Outline each Plasmodium ovale-infected red blood cell.
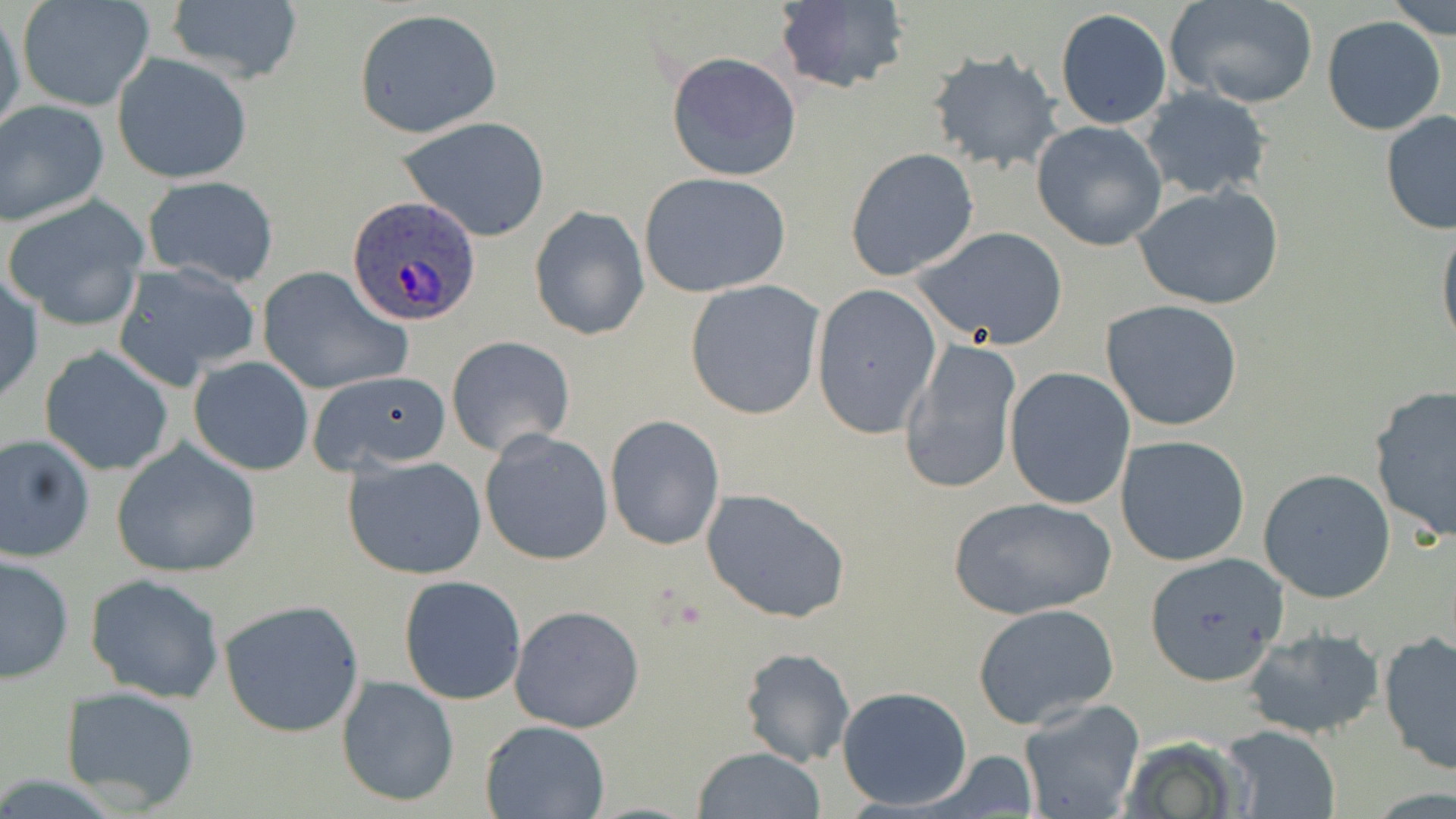

Approximate bounding boxes as (x1,y1)-(x2,y2) corner pairs in pixels.
Plasmodium ovale-infected red blood cells: (346,196)-(483,326).

slide_level_diagnosis: Plasmodium ovale
stain: May-Grünwald-Giemsa
field_of_view: single
modality: light microscopy
preparation: thin blood film
image_size: 1456×819 pixels
uninfected_red_blood_cell_locations: 'approximate bounding boxes as (x1,y1)-(x2,y2) corner pairs in pixels: (772,0)-(911,95), (1163,0)-(1319,109), (1384,0)-(1454,41), (162,1)-(305,84), (14,4)-(154,113), (0,8)-(25,146), (352,8)-(502,138), (1054,8)-(1171,129), (1321,16)-(1448,137), (927,50)-(1064,173), (666,51)-(803,181), (113,54)-(252,185), (1137,86)-(1274,200), (0,102)-(108,225), (1379,109)-(1456,234), (397,115)-(552,242), (1031,120)-(1168,250), (845,148)-(980,283), (638,172)-(792,298), (142,176)-(280,287), (1132,185)-(1284,310), (2,194)-(152,331), (529,206)-(650,342), (1436,220)-(1456,355), (913,226)-(1069,349), (112,261)-(261,390), (256,265)-(412,396), (1,274)-(43,409), (685,280)-(824,420), (811,283)-(941,437), (1100,299)-(1244,432), (446,335)-(576,460), (900,338)-(1023,496), (39,345)-(175,474), (188,356)-(315,476), (1005,366)-(1136,509), (304,369)-(456,475), (1368,385)-(1455,542), (605,414)-(726,549), (481,430)-(613,566), (0,434)-(95,563), (1116,435)-(1251,567), (110,438)-(264,578), (342,453)-(488,580), (1259,468)-(1396,602), (701,487)-(850,623), (948,496)-(1118,619), (1,552)-(74,683), (1144,552)-(1288,684), (85,573)-(226,704), (398,575)-(526,705), (218,598)-(366,737), (972,603)-(1120,730), (509,604)-(645,734), (1242,626)-(1386,741), (1378,634)-(1456,776), (739,646)-(854,768), (334,674)-(459,808), (59,685)-(200,812), (837,686)-(973,811), (1017,698)-(1147,819), (478,718)-(609,819), (1223,726)-(1342,817), (690,746)-(826,818)'
magnification: 1000x